Report the malaria status of this cell.
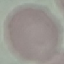

Uninfected.

Summary:
  - Capture: smartphone through the microscope eyepiece
  - Preparation: thin blood film
  - Stain: Giemsa
  - Image type: cell patch, automatically extracted from a larger field of view and resized to 64 × 64 pixels